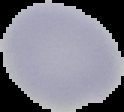

image type = segmented cell region on a black background
malaria status = uninfected
preparation = thin blood film
image size = 124×112 pixels